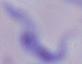
1000x magnification. A trypanosome is shown. Micrograph.